Name the parasite shown.
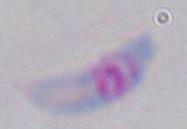
This is Toxoplasma gondii.

magnification = 1000x
modality = micrograph